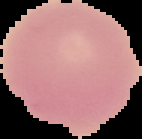

Summary:
  - Malaria status: uninfected
  - Image type: segmented cell region with the area outside set to black
  - Image size: 142×139 pixels
  - Preparation: thin blood film